Locate and identify every blood parasite.
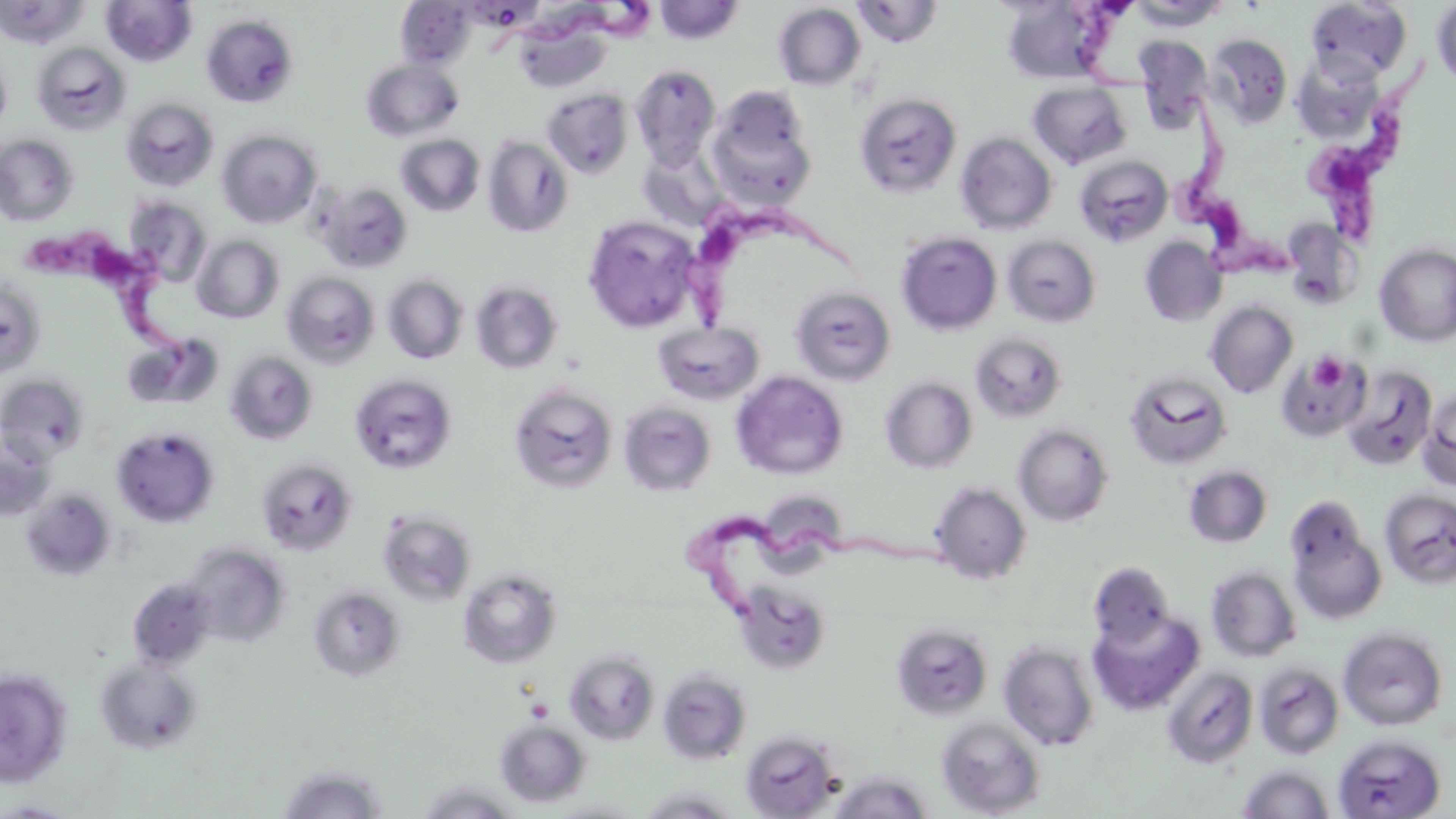
Approximate bounding boxes as [x1, y1, x2, y2] in pixels.
Trypanosoma brucei: [481, 2, 668, 57], [1074, 2, 1168, 94], [1310, 65, 1428, 257], [1170, 100, 1292, 288], [682, 199, 865, 329], [19, 227, 194, 393], [686, 503, 965, 632].
No Plasmodium falciparum, Plasmodium ovale, Plasmodium malariae, Plasmodium vivax, or Babesia divergens observed.

slide_level_diagnosis: Trypanosoma brucei
uninfected_red_blood_cell_locations: 'approximate bounding boxes as [x1, y1, x2, y2] in pixels: [101, 0, 197, 67], [1305, 0, 1412, 84], [0, 1, 87, 49], [396, 1, 477, 69], [653, 1, 745, 45], [851, 1, 943, 48], [1000, 1, 1112, 84], [1128, 1, 1230, 31], [1431, 1, 1456, 88], [772, 3, 866, 91], [201, 14, 298, 108], [514, 20, 611, 94], [1205, 34, 1293, 128], [1133, 36, 1213, 129], [31, 42, 131, 135], [0, 51, 12, 134], [360, 58, 464, 142], [1299, 58, 1375, 139], [632, 65, 721, 168], [1027, 81, 1131, 169], [705, 86, 817, 208], [542, 88, 633, 178], [854, 93, 961, 198], [120, 96, 220, 192], [217, 128, 322, 229], [956, 132, 1057, 235], [0, 134, 79, 226], [396, 134, 485, 216], [482, 135, 574, 238], [1073, 154, 1173, 248], [315, 182, 413, 274], [124, 195, 214, 286], [582, 214, 705, 334], [1281, 218, 1361, 308], [896, 231, 1002, 335], [192, 235, 285, 324], [1002, 235, 1101, 328], [1139, 236, 1228, 326], [1373, 242, 1456, 348], [282, 272, 380, 369], [382, 274, 469, 364], [0, 278, 47, 378], [470, 280, 564, 375], [790, 285, 896, 386], [1205, 301, 1299, 399], [652, 321, 766, 405], [122, 332, 224, 411], [969, 333, 1068, 423], [1276, 349, 1371, 443], [224, 351, 318, 445], [1340, 365, 1438, 471], [1123, 368, 1233, 471], [730, 370, 848, 481], [0, 371, 92, 462], [349, 372, 459, 475], [880, 377, 978, 474], [508, 383, 619, 495], [1419, 388, 1456, 490], [618, 401, 717, 497], [1013, 423, 1114, 527], [111, 424, 220, 528], [0, 430, 56, 521], [256, 457, 359, 556], [1183, 464, 1273, 549], [927, 481, 1032, 584], [1379, 487, 1456, 588], [21, 488, 117, 581], [757, 502, 847, 578], [376, 509, 477, 607], [1287, 518, 1387, 625], [182, 542, 292, 649], [1087, 561, 1176, 648], [1206, 565, 1301, 662], [457, 566, 563, 669], [127, 578, 217, 671], [732, 579, 834, 676], [307, 584, 407, 682], [1089, 608, 1205, 716], [890, 622, 993, 721], [1337, 625, 1448, 731], [998, 639, 1099, 751], [564, 649, 660, 746], [94, 656, 203, 755], [1253, 662, 1344, 759], [1160, 666, 1258, 768], [0, 668, 73, 787], [657, 668, 752, 765], [936, 717, 1046, 817], [494, 719, 590, 807], [740, 730, 841, 818], [1333, 734, 1446, 818], [275, 762, 390, 819], [1237, 764, 1335, 818], [827, 770, 934, 818], [413, 782, 527, 819], [635, 785, 743, 818], [0, 799, 83, 817], [545, 799, 649, 818]'
field_of_view: single
image_size: 1456×819 pixels
modality: optical microscopy
platelet_locations: 'approximate bounding boxes as [x1, y1, x2, y2] in pixels: [1308, 352, 1348, 391]'
preparation: thin blood smear
stain: May-Grünwald-Giemsa
magnification: 1000x